Outline each uninfected red blood cell.
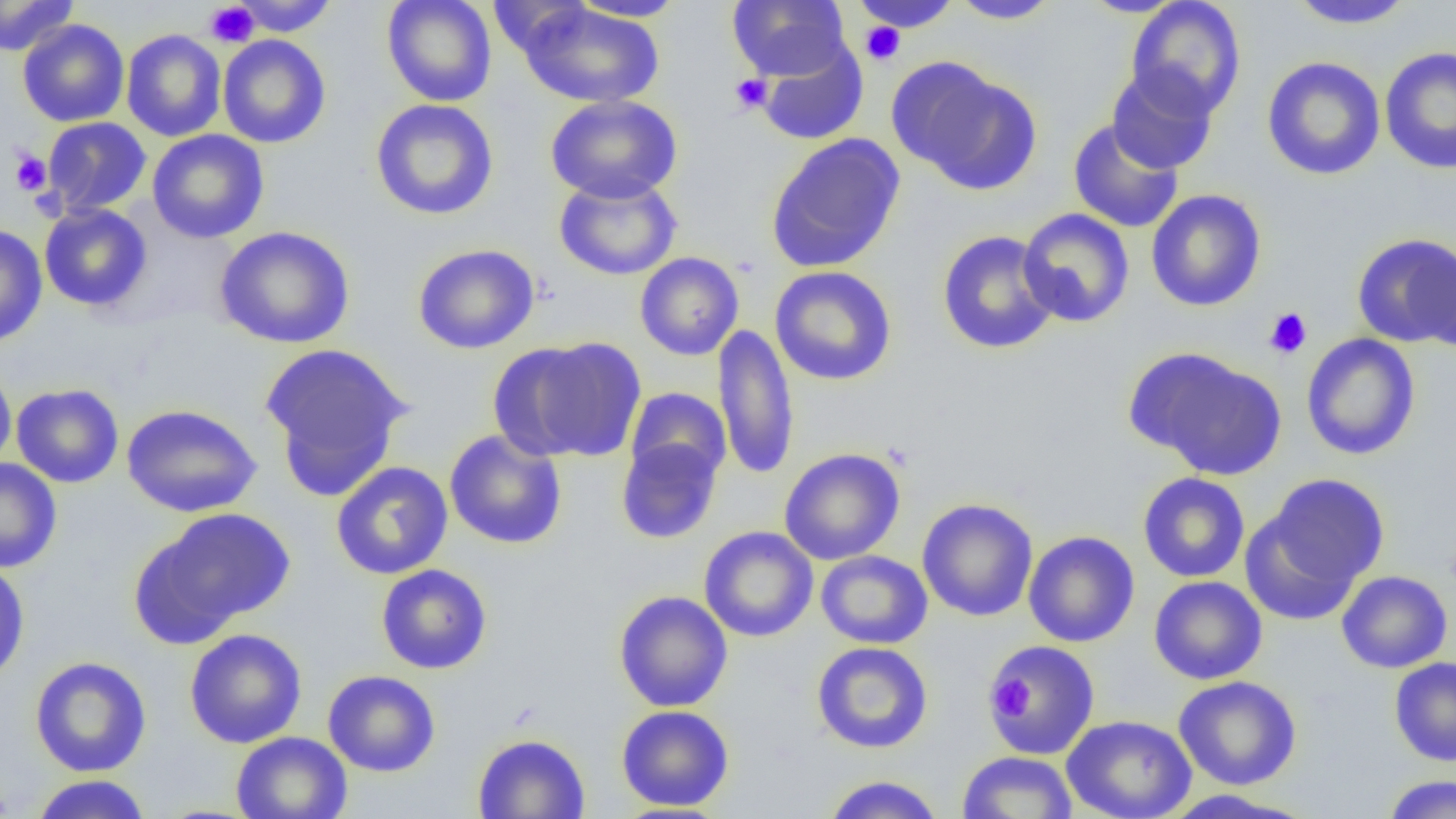

Approximate bounding boxes as (x1,y1)-(x2,y2) corner pairs in pixels.
Uninfected red blood cells: (0,0)-(79,57), (230,0)-(339,36), (381,0)-(497,107), (568,0)-(686,21), (728,0)-(850,81), (949,0)-(1062,24), (1078,0)-(1189,18), (1126,0)-(1246,119), (1285,0)-(1416,29), (850,1)-(962,33), (516,3)-(666,108), (17,19)-(129,127), (122,30)-(227,141), (218,34)-(331,148), (756,40)-(868,146), (1380,47)-(1456,175), (1261,56)-(1386,181), (891,59)-(1041,193), (1106,66)-(1219,174), (545,94)-(683,203), (370,98)-(499,220), (41,117)-(151,216), (1068,119)-(1184,233), (147,129)-(269,244), (765,133)-(905,274), (554,175)-(681,281), (1146,189)-(1266,312), (39,203)-(153,311), (1017,208)-(1135,327), (0,224)-(47,347), (214,226)-(355,349), (936,230)-(1060,355), (1351,233)-(1456,348), (411,244)-(540,355), (1417,244)-(1456,353), (634,252)-(745,361), (770,266)-(897,386), (713,324)-(800,481), (1301,333)-(1421,460), (494,338)-(647,463), (259,342)-(412,499), (1129,348)-(1287,480), (0,361)-(16,472), (11,383)-(124,488), (625,387)-(731,486), (122,403)-(262,517), (444,430)-(567,549), (615,435)-(724,544), (779,448)-(905,565), (0,458)-(63,573), (331,461)-(453,579), (1138,472)-(1250,582), (1257,473)-(1390,601), (917,498)-(1038,622), (141,508)-(296,635), (698,526)-(818,642), (1023,531)-(1139,648), (815,550)-(932,649), (0,558)-(30,686), (376,563)-(492,674), (1336,570)-(1452,673), (1149,576)-(1267,685), (613,590)-(733,712), (184,628)-(307,748), (985,639)-(1101,760), (811,642)-(933,754), (29,656)-(152,777), (1389,656)-(1456,766), (323,670)-(440,777), (1173,675)-(1302,790), (616,705)-(735,811), (1061,715)-(1197,819), (231,731)-(352,819), (472,732)-(590,818), (958,751)-(1077,818), (29,774)-(152,818), (821,774)-(945,819), (1382,774)-(1456,818), (1157,789)-(1315,818).

slide_level_diagnosis: no evidence of blood parasites
image_size: 1456×819 pixels
preparation: thin blood film
magnification: 1000x
platelet_locations: 'approximate bounding boxes as (x1,y1)-(x2,y2) corner pairs in pixels: (204,2)-(258,48), (860,21)-(905,66), (730,73)-(773,114), (11,150)-(52,195), (1264,307)-(1312,359), (986,672)-(1033,719)'
field_of_view: one of a larger specimen
modality: optical microscopy